Report the malaria status of this cell.
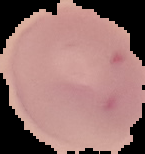

It is uninfected.

Summary:
  - Preparation: thin blood smear
  - Image type: segmented cell region with the area outside set to black
  - Image size: 145×154 pixels